Classify this cell by malaria status.
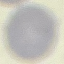
It is uninfected.

Summary:
  - Capture: smartphone through the microscope eyepiece
  - Image type: cell patch, automatically extracted from a larger field of view and resized to 64 × 64 pixels
  - Stain: Giemsa
  - Preparation: thin blood smear